Describe the morphology of the red blood cells.
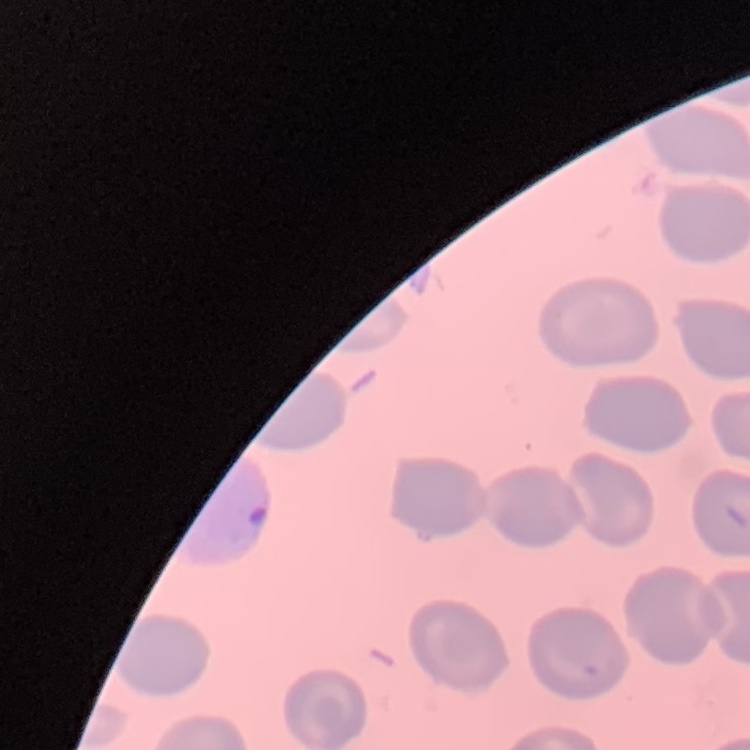
They show no rouleaux formation.

Field's or Giemsa stain. One tile cut from a larger photomicrograph. Thin peripheral smear.